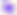
modality: micrograph
identification: Toxoplasma gondii
magnification: 400x